Locate every blood parasite and identify its species.
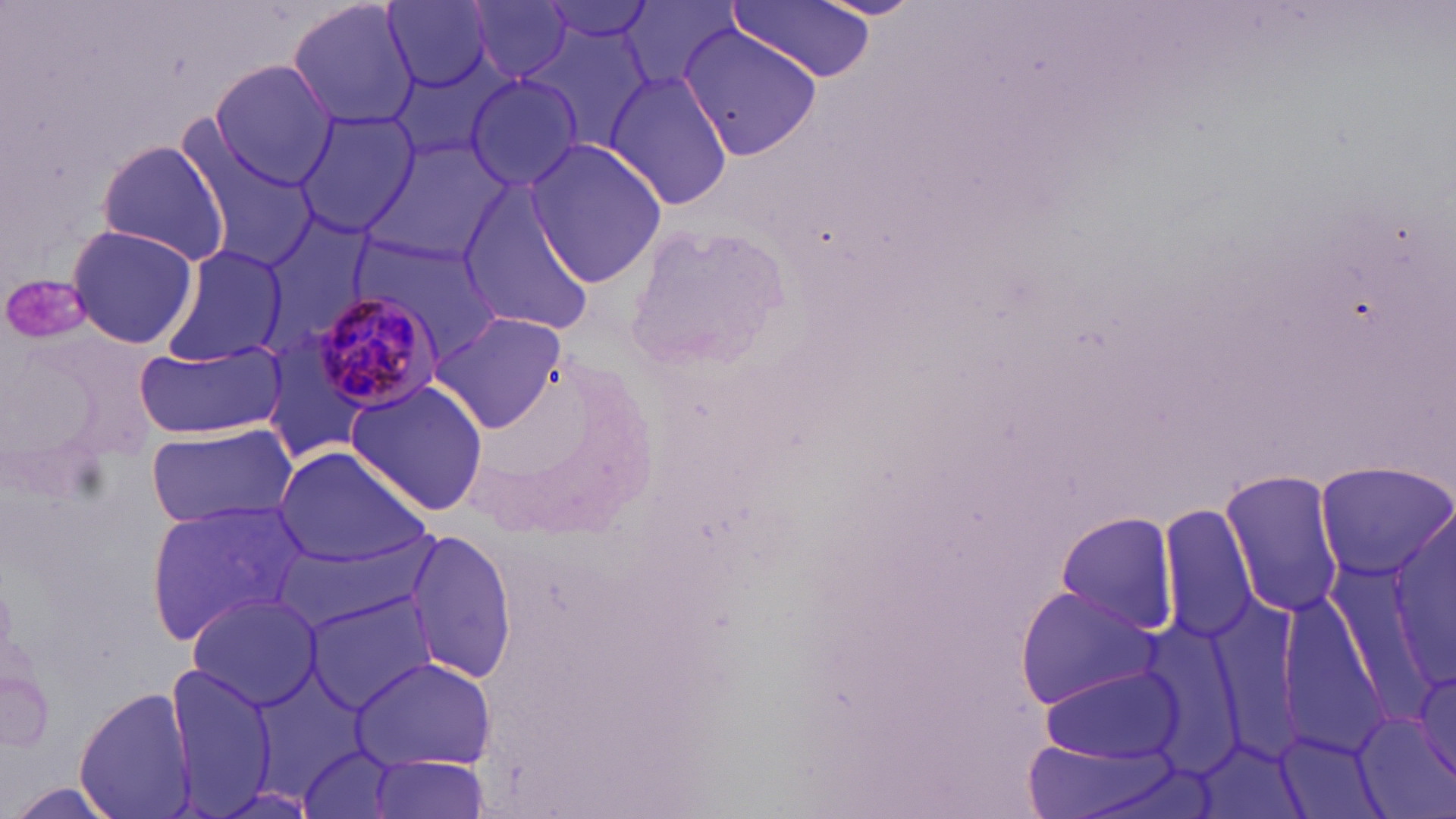
Approximate bounding boxes as named x1/y1/x2/y2 corners in pixels.
Plasmodium malariae-infected red blood cells: (x1=302, y1=289, x2=449, y2=420).
No Plasmodium falciparum, Plasmodium ovale, Plasmodium vivax, Babesia divergens, or Trypanosoma brucei observed.

slide-level diagnosis = Plasmodium malariae
image size = 1456×819 pixels
uninfected red blood cell locations = approximate bounding boxes as named x1/y1/x2/y2 corners in pixels: (x1=286, y1=0, x2=419, y2=132), (x1=467, y1=0, x2=575, y2=84), (x1=733, y1=0, x2=878, y2=86), (x1=536, y1=1, x2=660, y2=49), (x1=381, y1=2, x2=499, y2=93), (x1=616, y1=3, x2=740, y2=92), (x1=527, y1=24, x2=657, y2=151), (x1=677, y1=24, x2=819, y2=163), (x1=206, y1=60, x2=337, y2=188), (x1=604, y1=69, x2=733, y2=211), (x1=464, y1=74, x2=584, y2=192), (x1=293, y1=107, x2=415, y2=237), (x1=187, y1=132, x2=321, y2=274), (x1=93, y1=138, x2=231, y2=265), (x1=524, y1=139, x2=667, y2=288), (x1=362, y1=143, x2=507, y2=267), (x1=454, y1=178, x2=598, y2=337), (x1=258, y1=212, x2=372, y2=349), (x1=64, y1=223, x2=199, y2=350), (x1=352, y1=229, x2=503, y2=359), (x1=159, y1=245, x2=288, y2=367), (x1=430, y1=312, x2=566, y2=433), (x1=135, y1=340, x2=287, y2=440), (x1=343, y1=379, x2=489, y2=516), (x1=143, y1=421, x2=298, y2=529), (x1=272, y1=446, x2=431, y2=569), (x1=1315, y1=463, x2=1456, y2=581), (x1=1219, y1=470, x2=1346, y2=618), (x1=145, y1=500, x2=306, y2=643), (x1=1160, y1=503, x2=1259, y2=644), (x1=1389, y1=507, x2=1454, y2=687), (x1=1056, y1=511, x2=1177, y2=636), (x1=401, y1=528, x2=515, y2=686), (x1=275, y1=539, x2=425, y2=627), (x1=1013, y1=585, x2=1164, y2=707), (x1=186, y1=593, x2=324, y2=710), (x1=305, y1=597, x2=439, y2=713), (x1=1405, y1=654, x2=1456, y2=794), (x1=351, y1=655, x2=495, y2=772), (x1=164, y1=665, x2=279, y2=816), (x1=1037, y1=666, x2=1182, y2=768), (x1=74, y1=684, x2=197, y2=819), (x1=296, y1=744, x2=403, y2=819), (x1=364, y1=754, x2=492, y2=819)
stain = May-Grünwald-Giemsa
platelet locations = approximate bounding boxes as named x1/y1/x2/y2 corners in pixels: (x1=6, y1=279, x2=102, y2=342)
field of view = one of a larger specimen
modality = optical microscopy
magnification = 1000x
preparation = thin blood smear